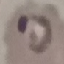

Malaria status: parasitized. Acquired by smartphone through the microscope eyepiece. Giemsa-stained preparation. Cell patch, automatically extracted from a larger field of view and resized to 64 × 64 pixels. Thin blood film.